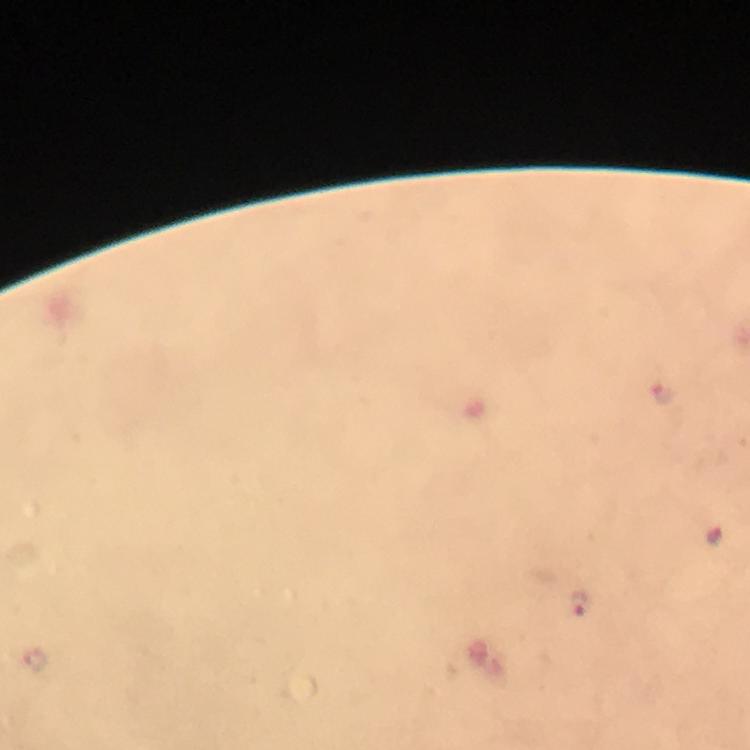
magnification = 100x
cropped from = a single field of view
capture = smartphone camera through the microscope
immersion oil = used
malaria parasite locations = approximate object centers, in pixels from the top-left corner: (x=666, y=394), (x=717, y=538), (x=578, y=602)
image size = 750×750 pixels
stain = Giemsa
context = from a malaria diagnostic workup
preparation = thick smear